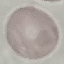
Summary:
  - Result: negative for malaria parasites
  - Capture: smartphone through the microscope eyepiece
  - Image type: cell patch, automatically extracted from a larger field of view and resized to 64 × 64 pixels
  - Stain: Giemsa
  - Preparation: thin smear